Report the malaria status of this cell.
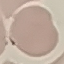

It is uninfected.

preparation: thin blood smear
capture: smartphone through the microscope eyepiece
stain: Giemsa
image_type: automatically extracted cell patch, resized to 64 × 64 pixels